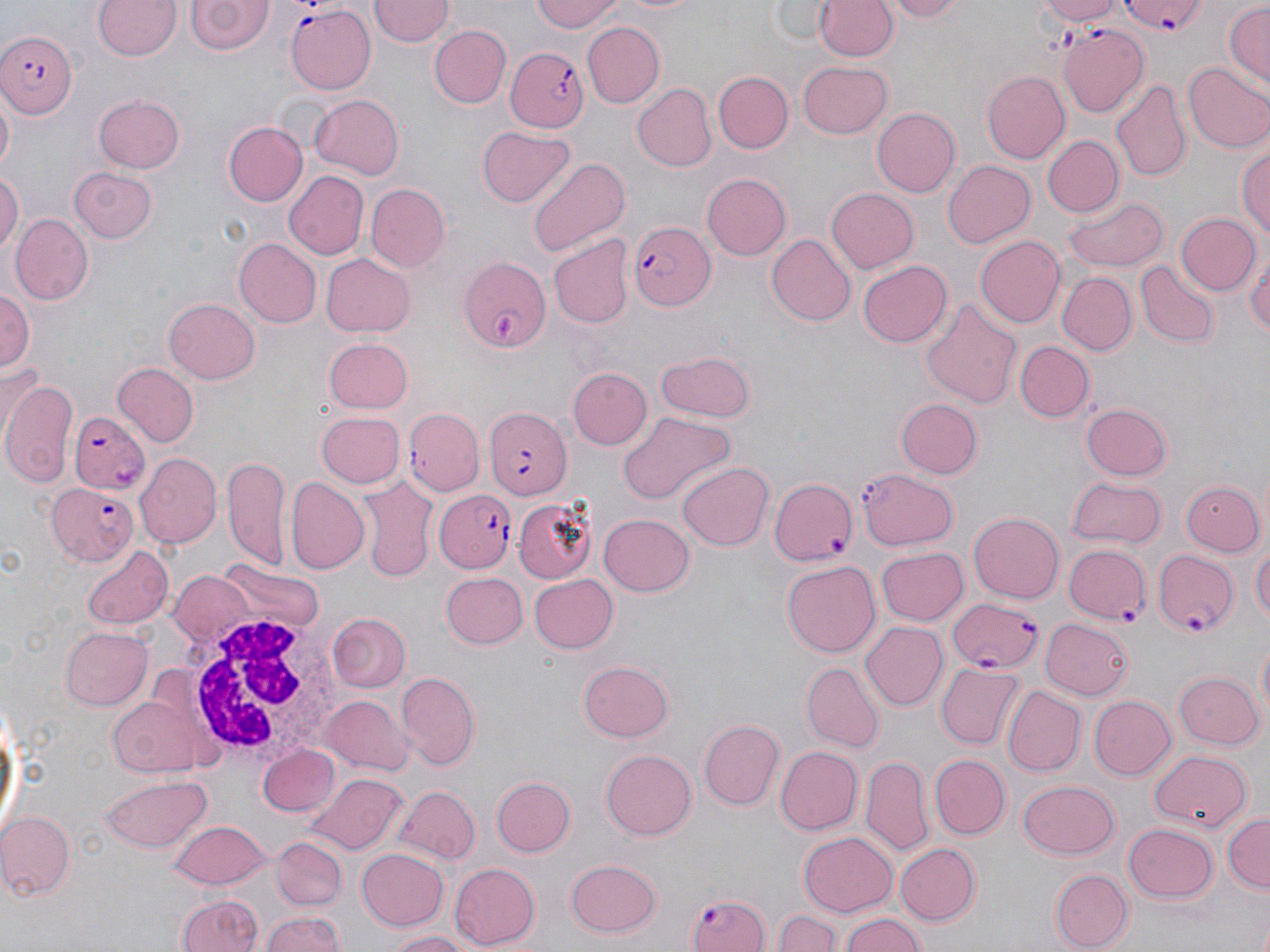

{
  "slide_level_diagnosis": "Plasmodium falciparum",
  "uninfected_red_blood_cell_locations": "approximate bounding boxes as (x1, y1, x2, y2) in pixels: (94, 0, 181, 61), (530, 0, 626, 33), (610, 0, 705, 17), (771, 0, 837, 43), (810, 0, 902, 60), (881, 0, 972, 22), (1032, 0, 1121, 26), (185, 1, 274, 56), (369, 1, 453, 47), (1224, 2, 1269, 88), (583, 23, 666, 106), (429, 25, 512, 108), (800, 61, 894, 138), (1185, 61, 1270, 153), (712, 70, 794, 154), (983, 70, 1070, 163), (1112, 81, 1190, 182), (631, 82, 716, 172), (93, 93, 186, 173), (1, 94, 15, 175), (308, 95, 404, 179), (872, 106, 960, 198), (223, 122, 306, 206), (475, 126, 574, 209), (1044, 135, 1121, 215), (1237, 136, 1269, 246), (527, 157, 633, 261), (942, 160, 1037, 249), (69, 167, 159, 243), (0, 170, 22, 258), (282, 170, 368, 261), (702, 173, 791, 261), (365, 183, 450, 272), (825, 187, 919, 273), (1064, 196, 1168, 273), (1175, 212, 1259, 297), (11, 215, 94, 304), (768, 233, 856, 326), (549, 235, 633, 328), (976, 235, 1066, 329), (232, 237, 321, 329), (1246, 249, 1270, 344), (320, 252, 415, 338), (858, 260, 953, 347), (1138, 261, 1219, 347), (1058, 272, 1136, 355), (1, 284, 35, 379), (164, 297, 260, 383), (922, 298, 1023, 409), (326, 336, 413, 413), (1014, 340, 1094, 422), (656, 351, 756, 422), (111, 361, 199, 447), (568, 368, 652, 450), (1, 375, 76, 486), (897, 398, 982, 478), (1081, 403, 1174, 480), (406, 408, 483, 495), (316, 410, 405, 488), (615, 412, 734, 504), (136, 454, 221, 549), (221, 455, 292, 569), (676, 462, 771, 552), (856, 468, 961, 550), (285, 476, 369, 572), (1179, 476, 1265, 558), (359, 479, 434, 580), (1068, 480, 1166, 548), (513, 494, 600, 583), (968, 512, 1065, 604), (598, 514, 693, 598), (1252, 543, 1269, 627), (84, 545, 172, 630), (877, 548, 967, 626), (781, 559, 881, 657), (218, 560, 320, 633), (169, 571, 259, 653), (440, 572, 528, 648), (528, 573, 619, 653), (331, 614, 411, 692), (1042, 618, 1133, 698), (861, 623, 948, 711), (60, 626, 151, 710), (579, 660, 675, 741), (804, 662, 883, 751), (936, 664, 1022, 748), (945, 668, 1088, 762), (1173, 671, 1263, 751), (393, 673, 479, 770), (1001, 685, 1084, 776), (106, 691, 214, 777), (1089, 695, 1177, 781), (323, 696, 416, 776), (0, 698, 22, 844), (699, 720, 783, 810), (773, 745, 862, 833), (257, 747, 338, 818), (600, 749, 697, 841), (1149, 751, 1252, 832), (931, 754, 1010, 839), (861, 756, 932, 856), (307, 774, 408, 854), (101, 775, 212, 854), (492, 775, 575, 856), (1018, 779, 1120, 860), (394, 786, 480, 865), (1, 811, 75, 899), (1223, 812, 1269, 894), (166, 820, 270, 888), (1124, 823, 1218, 902), (798, 833, 898, 915), (270, 836, 348, 911), (894, 843, 979, 925), (357, 847, 450, 932), (566, 857, 662, 937), (449, 863, 542, 948), (1050, 870, 1131, 950), (175, 893, 263, 952), (839, 909, 928, 952), (776, 910, 842, 952), (260, 911, 347, 952), (385, 930, 479, 951)",
  "field_of_view": "single",
  "image_size": "1270×952 pixels",
  "magnification": "1000x",
  "preparation": "thin blood smear",
  "white_blood_cell_locations": "approximate bounding boxes as (x1, y1, x2, y2) in pixels: (183, 608, 350, 768)",
  "modality": "optical microscopy",
  "stain": "May-Grünwald-Giemsa",
  "plasmodium_falciparum_infected_red_blood_cell_locations": "approximate bounding boxes as (x1, y1, x2, y2) in pixels: (1121, 0, 1209, 37), (285, 3, 377, 93), (1059, 26, 1150, 116), (0, 29, 77, 118), (505, 45, 589, 133), (629, 220, 716, 310), (458, 255, 551, 352), (484, 408, 573, 500), (69, 410, 149, 494), (770, 478, 858, 565), (46, 481, 139, 566), (434, 488, 516, 575), (1063, 542, 1153, 625), (1154, 545, 1241, 639), (947, 596, 1044, 674), (686, 890, 770, 951)"
}